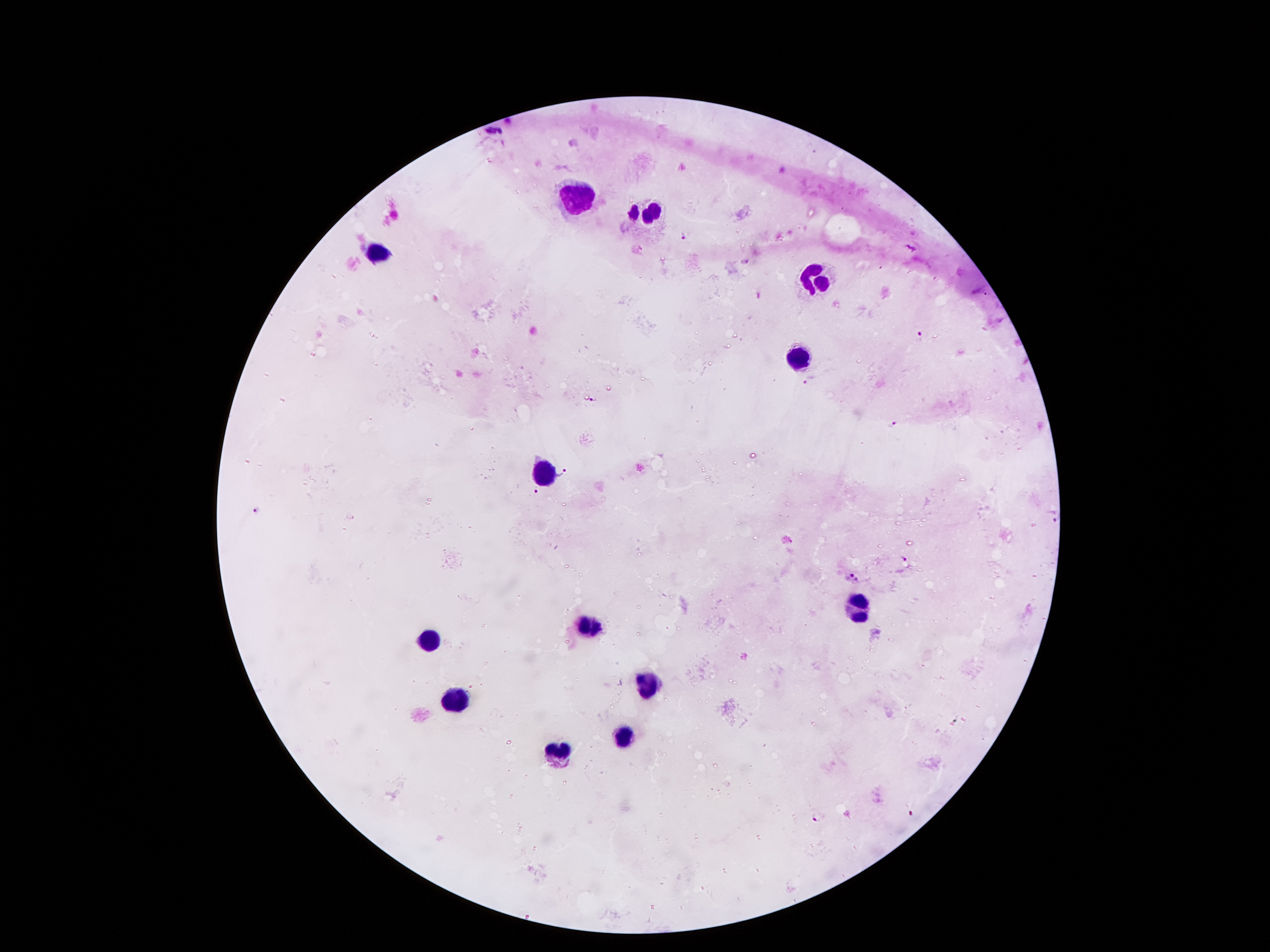
Approximate centers as {x, y} in pixels. Leukocyte locations: {575, 202}, {649, 214}, {376, 255}, {817, 274}, {802, 360}, {540, 470}, {858, 610}, {587, 627}, {428, 640}, {646, 684}, {453, 699}, {625, 737}, {553, 755}. Malaria parasite locations: {632, 214}, {683, 236}, {745, 260}, {759, 295}, {921, 336}, {807, 381}, {593, 399}, {892, 425}, {564, 473}, {535, 491}, {257, 509}, {903, 558}, {855, 577}, {912, 814}, {819, 818}. Patient malaria status: infected with Plasmodium falciparum. Smartphone photograph taken through the microscope eyepiece. Thick blood smear. Giemsa-stained preparation. 100x magnification. One field from this slide. Image is 1270×952 pixels.